Give the preparation type.
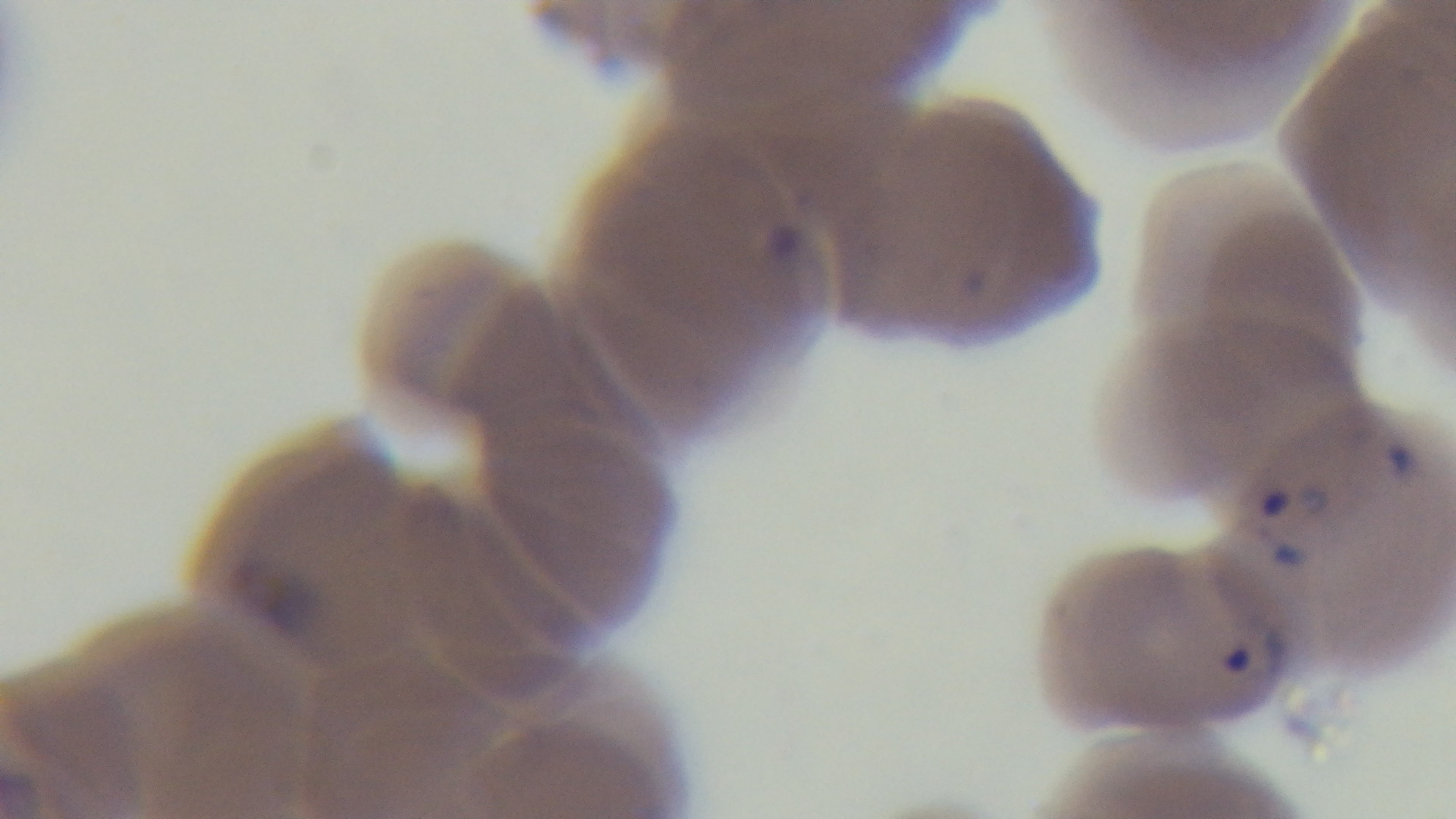
Thin.

Summary:
  - Modality: light microscopy
  - Field of view: one from the slide
  - Capture: mounted 4K digital camera
  - Objective: 100x oil immersion
  - Stain: Giemsa
  - Malaria status: positive